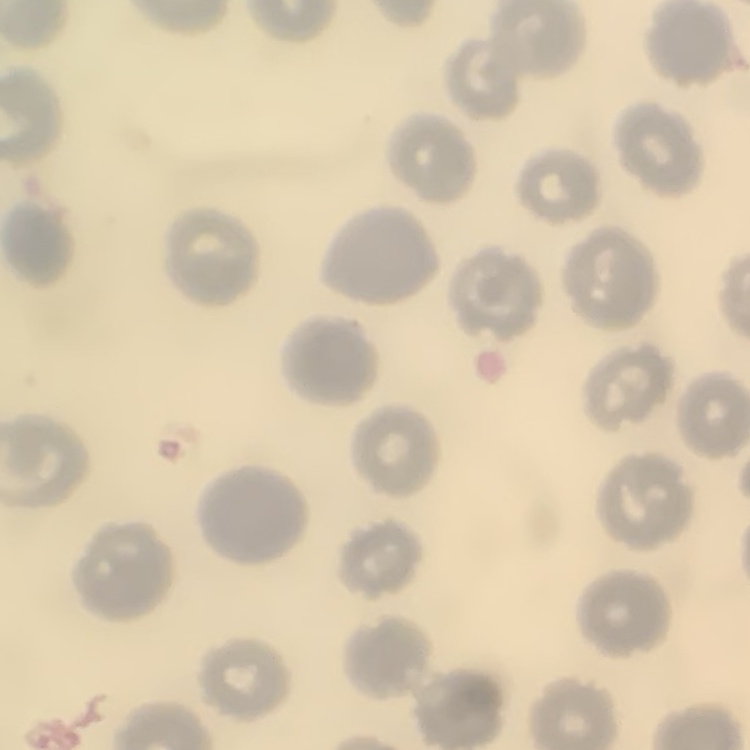 The erythrocytes exhibit no rouleaux formation. Square crop of a larger photomicrograph. Thin blood film. Stained with either Field's or Giemsa.